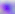

Photomicrograph. 400x magnification. Toxoplasma gondii is shown.